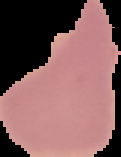
Segmented cell region on a black background. Malaria status: uninfected. From a thin blood film. Image is 121×157 pixels.